Identify the cell.
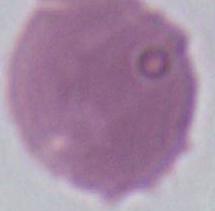

An erythrocyte.

modality = photomicrograph
magnification = 1000x